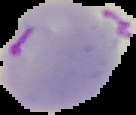
Summary:
  - Image type: segmented cell region with the area outside set to black
  - Malaria status: parasitized
  - Preparation: thin blood smear
  - Image size: 136×115 pixels